Outline every Plasmodium parasite, every leukocyte, and every artifact (stain precipitate or debris).
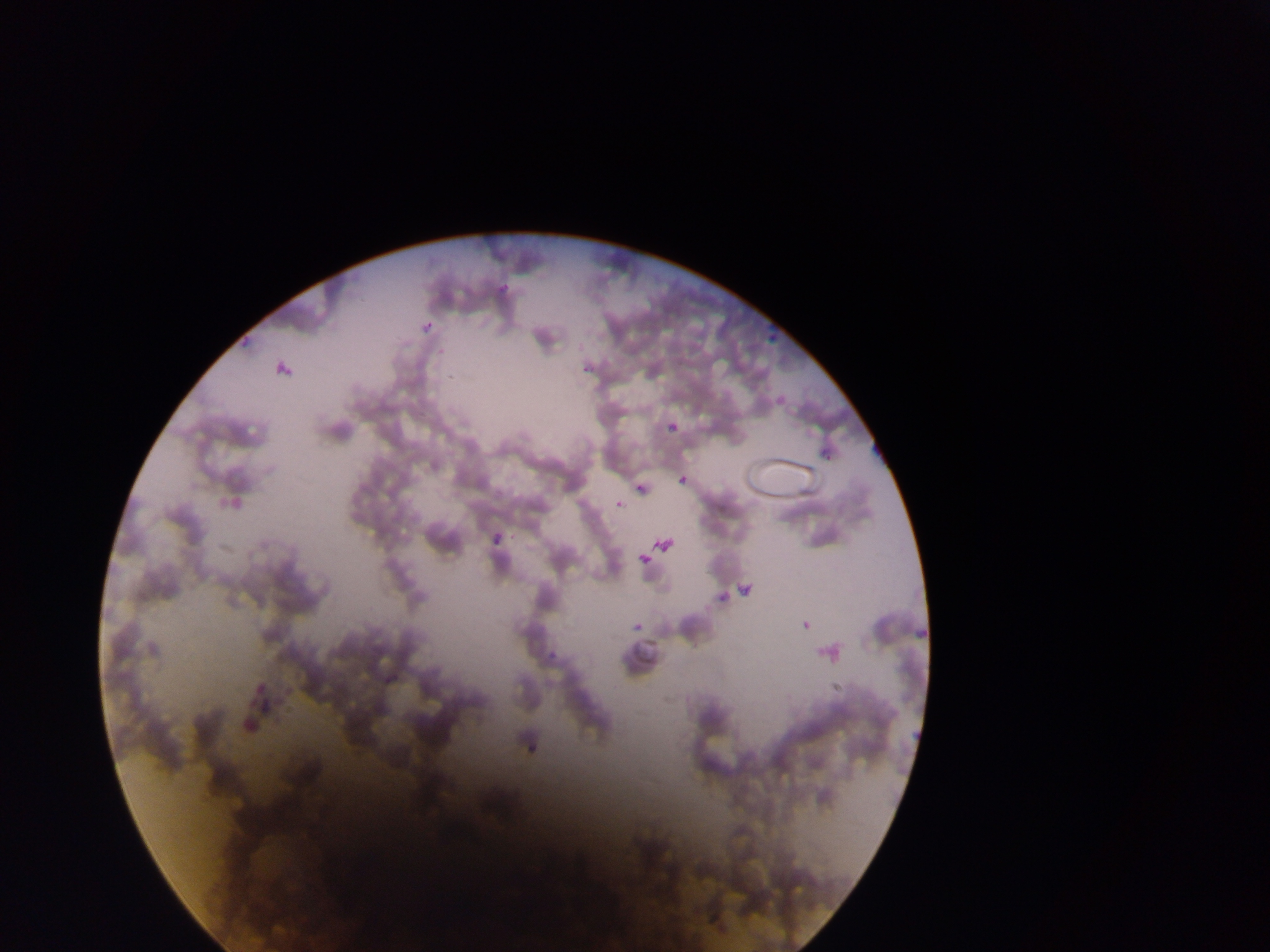
Approximate bounding boxes as {left, top, right, bottom} in pixels.
Plasmodium parasites: {491, 268, 511, 306}, {240, 319, 266, 357}, {415, 321, 435, 338}, {752, 332, 778, 347}, {266, 350, 301, 380}, {766, 383, 792, 411}, {663, 395, 688, 446}, {802, 418, 840, 464}, {653, 463, 689, 493}, {618, 469, 648, 504}, {614, 498, 625, 510}, {483, 509, 519, 554}, {653, 511, 688, 546}, {639, 552, 651, 565}, {738, 570, 759, 596}, {789, 583, 832, 631}, {699, 587, 720, 613}, {908, 608, 928, 649}, {541, 618, 582, 661}, {631, 621, 642, 632}, {824, 679, 850, 710}, {241, 683, 277, 721}, {518, 735, 539, 765}.
No leukocytes observed.

Photographed through a microscope with a mobile-phone camera. Image is 1270×952 pixels. Thin blood smear. Collected in Ghana. Single field of view.